Give the extent of all Plasmodium vivax-infected red blood cells.
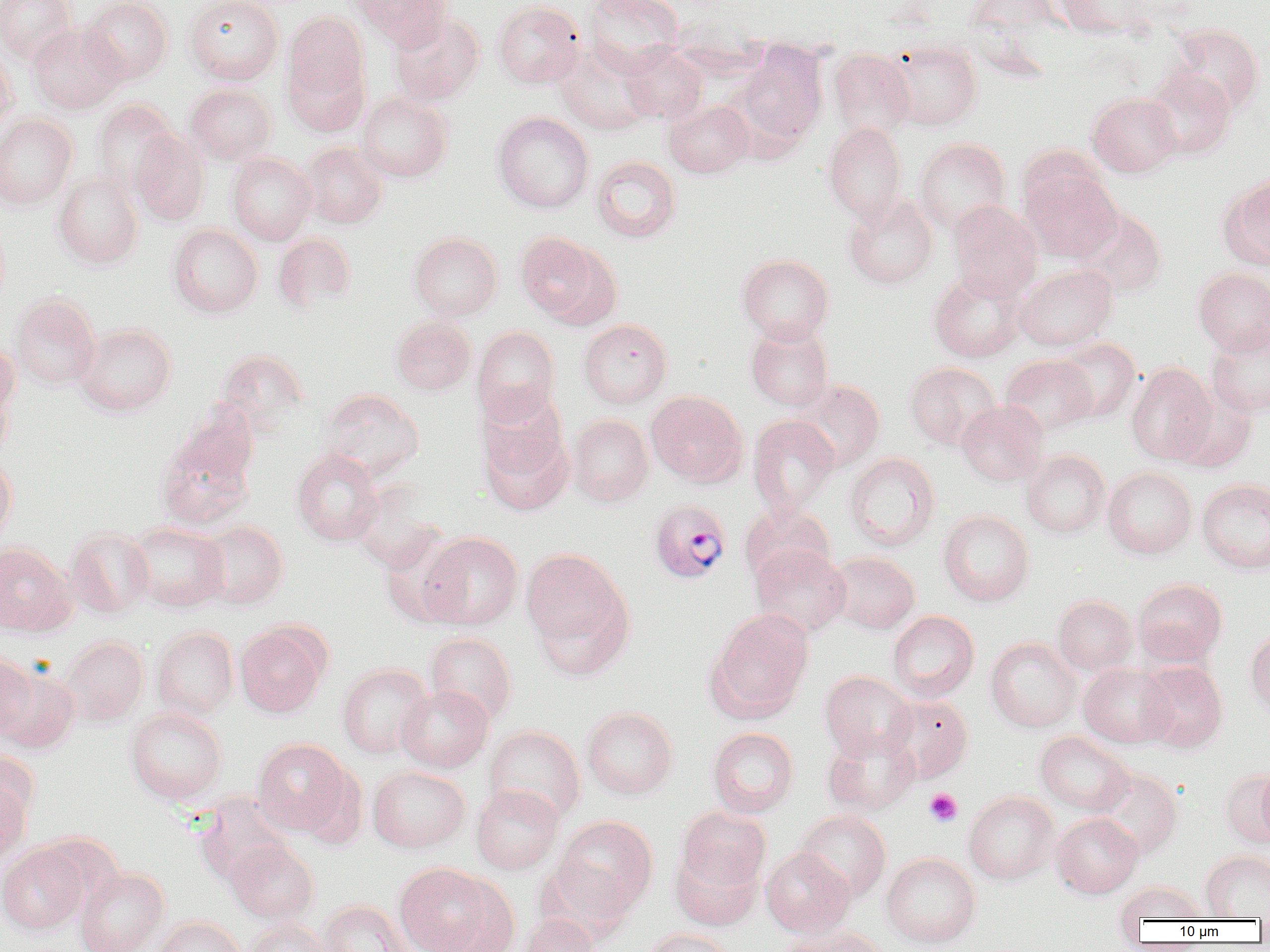
Approximate bounding boxes as [x1, y1, x2, y2] in pixels.
Plasmodium vivax-infected red blood cells: [649, 500, 731, 584].

slide-level diagnosis = Plasmodium vivax
field of view = single
image size = 1270×952 pixels
preparation = thin blood film
uninfected red blood cell locations = approximate bounding boxes as [x1, y1, x2, y2] in pixels: [0, 0, 77, 63], [80, 0, 173, 85], [185, 0, 284, 84], [352, 0, 451, 50], [583, 0, 684, 75], [965, 0, 1060, 35], [1054, 0, 1153, 38], [492, 1, 585, 89], [283, 12, 368, 101], [389, 13, 485, 105], [27, 23, 125, 114], [1167, 24, 1265, 116], [885, 40, 982, 130], [731, 42, 828, 155], [555, 43, 656, 135], [619, 43, 708, 124], [0, 46, 19, 132], [828, 49, 915, 139], [284, 55, 369, 137], [1143, 68, 1236, 160], [185, 83, 277, 165], [356, 92, 453, 182], [1087, 93, 1181, 177], [91, 100, 179, 192], [664, 101, 754, 178], [492, 112, 593, 213], [0, 114, 77, 210], [824, 123, 909, 222], [130, 131, 210, 226], [914, 138, 1011, 234], [300, 142, 387, 228], [227, 153, 316, 245], [591, 155, 681, 243], [1021, 169, 1121, 263], [54, 171, 144, 268], [1221, 175, 1270, 269], [843, 194, 938, 290], [948, 200, 1042, 300], [1075, 208, 1166, 297], [167, 224, 263, 317], [409, 232, 503, 320], [515, 232, 616, 326], [273, 233, 356, 314], [737, 254, 834, 344], [1014, 264, 1117, 351], [1193, 268, 1270, 355], [929, 270, 1027, 362], [10, 294, 101, 389], [391, 316, 476, 395], [579, 319, 672, 408], [745, 322, 834, 411], [75, 323, 176, 416], [1207, 325, 1270, 418], [472, 326, 560, 423], [1055, 339, 1140, 422], [0, 343, 18, 445], [215, 348, 310, 432], [1000, 355, 1098, 437], [904, 362, 1000, 450], [1126, 363, 1216, 464], [792, 380, 885, 471], [1171, 386, 1257, 473], [319, 388, 424, 479], [476, 389, 567, 483], [646, 391, 747, 487], [956, 400, 1048, 486], [566, 414, 654, 506], [748, 416, 839, 515], [155, 421, 258, 532], [479, 428, 573, 516], [291, 449, 383, 546], [1020, 450, 1111, 538], [844, 452, 940, 551], [0, 454, 17, 548], [1103, 467, 1197, 559], [1197, 479, 1270, 574], [350, 484, 441, 573], [740, 504, 835, 584], [939, 510, 1034, 606], [195, 521, 288, 609], [127, 522, 229, 612], [65, 527, 154, 619], [380, 530, 465, 627], [419, 532, 523, 630], [0, 542, 73, 636], [750, 545, 851, 636], [521, 548, 632, 660], [827, 552, 920, 634], [1132, 578, 1227, 666], [1053, 596, 1138, 676], [707, 609, 814, 720], [888, 611, 979, 701], [235, 623, 328, 717], [151, 626, 239, 719], [1246, 628, 1270, 720], [425, 632, 517, 724], [61, 636, 148, 725], [985, 637, 1081, 732], [0, 654, 39, 740], [1137, 661, 1228, 753], [337, 664, 433, 758], [1079, 664, 1175, 748], [1, 665, 80, 754], [819, 671, 916, 761], [396, 685, 493, 771], [884, 695, 973, 783], [125, 707, 227, 804], [581, 707, 678, 799], [484, 726, 585, 823], [707, 728, 799, 817], [822, 731, 919, 816], [1035, 732, 1134, 816], [252, 739, 352, 836], [1256, 765, 1270, 848], [368, 766, 470, 852], [1091, 767, 1183, 859], [1222, 769, 1270, 848], [0, 772, 32, 864], [471, 785, 563, 875], [964, 791, 1058, 884], [195, 794, 294, 885], [677, 807, 770, 893], [794, 810, 891, 902], [1051, 813, 1143, 898], [555, 816, 658, 915], [225, 839, 318, 924], [0, 844, 88, 934], [670, 848, 762, 931], [761, 848, 855, 938], [1201, 851, 1270, 919], [881, 853, 981, 948], [537, 857, 636, 943], [394, 863, 500, 952], [75, 867, 169, 952], [1116, 882, 1208, 923], [318, 900, 414, 952], [521, 914, 601, 952], [154, 916, 247, 952], [244, 919, 333, 952], [774, 926, 888, 952], [642, 929, 736, 952]
modality = optical microscopy
platelet locations = approximate bounding boxes as [x1, y1, x2, y2] in pixels: [924, 788, 962, 826]
magnification = 1000x